Assess this cell for malaria.
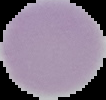

It is uninfected.

From a thin blood film. Image is 106×100 pixels. The area outside the segmented cell region is set to black.